Name the parasite shown.
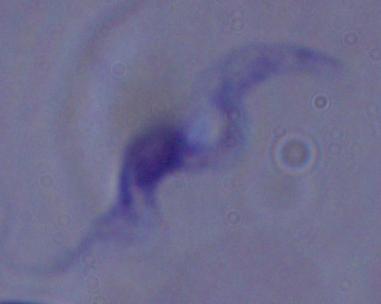
A trypanosome.

Summary:
  - Magnification: 1000x
  - Modality: micrograph